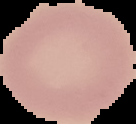

Image is 136×124 pixels. Cell region segmented out of the field of view; the surrounding area is masked to black. Malaria status: uninfected. From a thin blood smear.